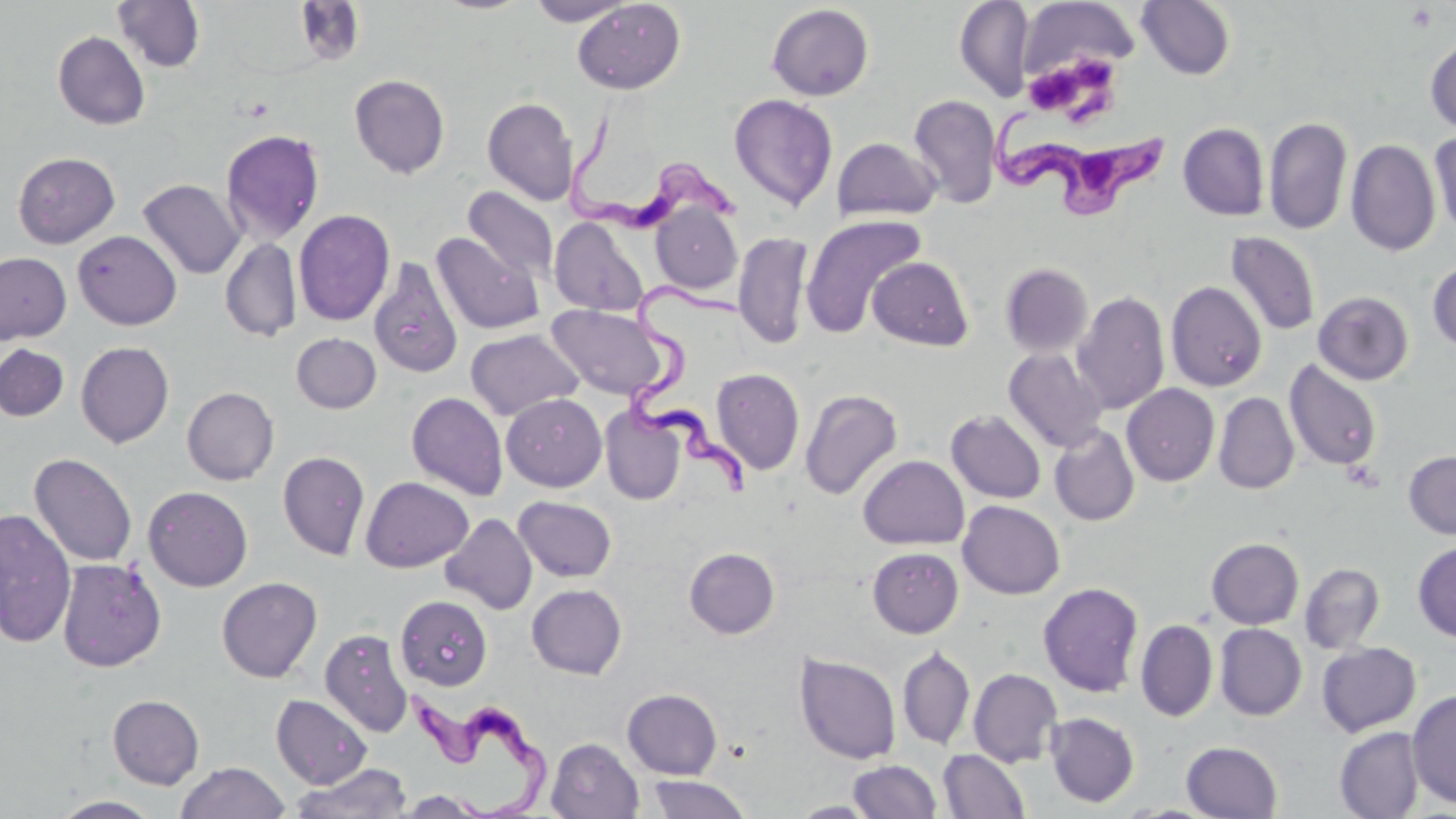
slide_level_diagnosis: Trypanosoma brucei
modality: optical microscopy
preparation: thin blood film
field_of_view: one of a larger specimen
trypanosoma_brucei_locations: 'approximate bounding boxes as (x1,y1)-(x2,y2) corner pairs in pixels: (559,98)-(752,238), (992,101)-(1170,222), (622,279)-(757,507), (397,680)-(558,818)'
image_size: 1456×819 pixels
uninfected_red_blood_cell_locations: 'approximate bounding boxes as (x1,y1)-(x2,y2) corner pairs in pixels: (112,0)-(206,73), (525,0)-(634,26), (571,0)-(686,94), (954,0)-(1035,102), (1136,0)-(1236,80), (1018,1)-(1139,82), (766,4)-(874,101), (52,31)-(151,130), (1425,36)-(1456,133), (349,74)-(450,179), (729,94)-(838,211), (908,94)-(1002,208), (482,97)-(579,206), (1264,116)-(1352,235), (1178,123)-(1270,220), (220,128)-(325,245), (1429,132)-(1456,237), (832,137)-(941,222), (1345,139)-(1440,256), (13,152)-(120,248), (137,179)-(245,280), (463,187)-(559,285), (651,203)-(742,295), (293,209)-(395,326), (800,213)-(926,337), (550,217)-(650,316), (73,230)-(181,330), (431,231)-(545,335), (733,231)-(813,350), (1225,232)-(1321,336), (219,237)-(302,343), (0,252)-(71,343), (867,257)-(974,351), (369,259)-(463,380), (1427,260)-(1456,352), (1000,263)-(1093,357), (1166,281)-(1267,392), (1071,291)-(1170,415), (1313,291)-(1414,385), (546,304)-(672,401), (465,328)-(584,421), (291,333)-(381,413), (75,341)-(174,448), (1,344)-(69,421), (1004,348)-(1108,453), (1284,359)-(1382,472), (712,368)-(804,475), (1122,384)-(1220,486), (182,387)-(279,485), (800,389)-(903,499), (406,392)-(508,500), (1214,392)-(1299,494), (502,393)-(607,492), (600,406)-(685,505), (946,410)-(1047,504), (1049,425)-(1140,526), (1403,450)-(1456,539), (278,451)-(370,560), (28,452)-(138,568), (858,455)-(969,550), (360,477)-(473,573), (143,486)-(253,592), (513,496)-(617,582), (957,500)-(1065,599), (0,508)-(77,647), (440,513)-(537,614), (1206,537)-(1304,629), (1413,542)-(1456,642), (684,547)-(780,639), (868,547)-(963,638), (57,558)-(166,671), (1299,562)-(1385,654), (216,577)-(322,682), (1038,582)-(1144,697), (526,584)-(627,679), (395,595)-(493,691), (1135,619)-(1218,722), (1214,623)-(1307,720), (320,628)-(414,737), (1316,642)-(1421,736), (897,646)-(975,749), (794,652)-(901,765), (968,668)-(1063,768), (622,688)-(723,779), (1407,689)-(1456,808), (108,694)-(204,789), (271,694)-(372,789), (1045,712)-(1139,807), (1334,727)-(1425,819), (546,738)-(643,819), (1181,741)-(1283,818), (938,749)-(1031,818), (849,760)-(941,818), (176,762)-(290,819), (290,762)-(413,819), (645,774)-(752,818), (393,790)-(494,817), (50,796)-(163,818), (790,801)-(881,818)'
magnification: 1000x
platelet_locations: 'approximate bounding boxes as (x1,y1)-(x2,y2) corner pairs in pixels: (1406,4)-(1438,31), (1022,60)-(1097,116)'
stain: May-Grünwald-Giemsa